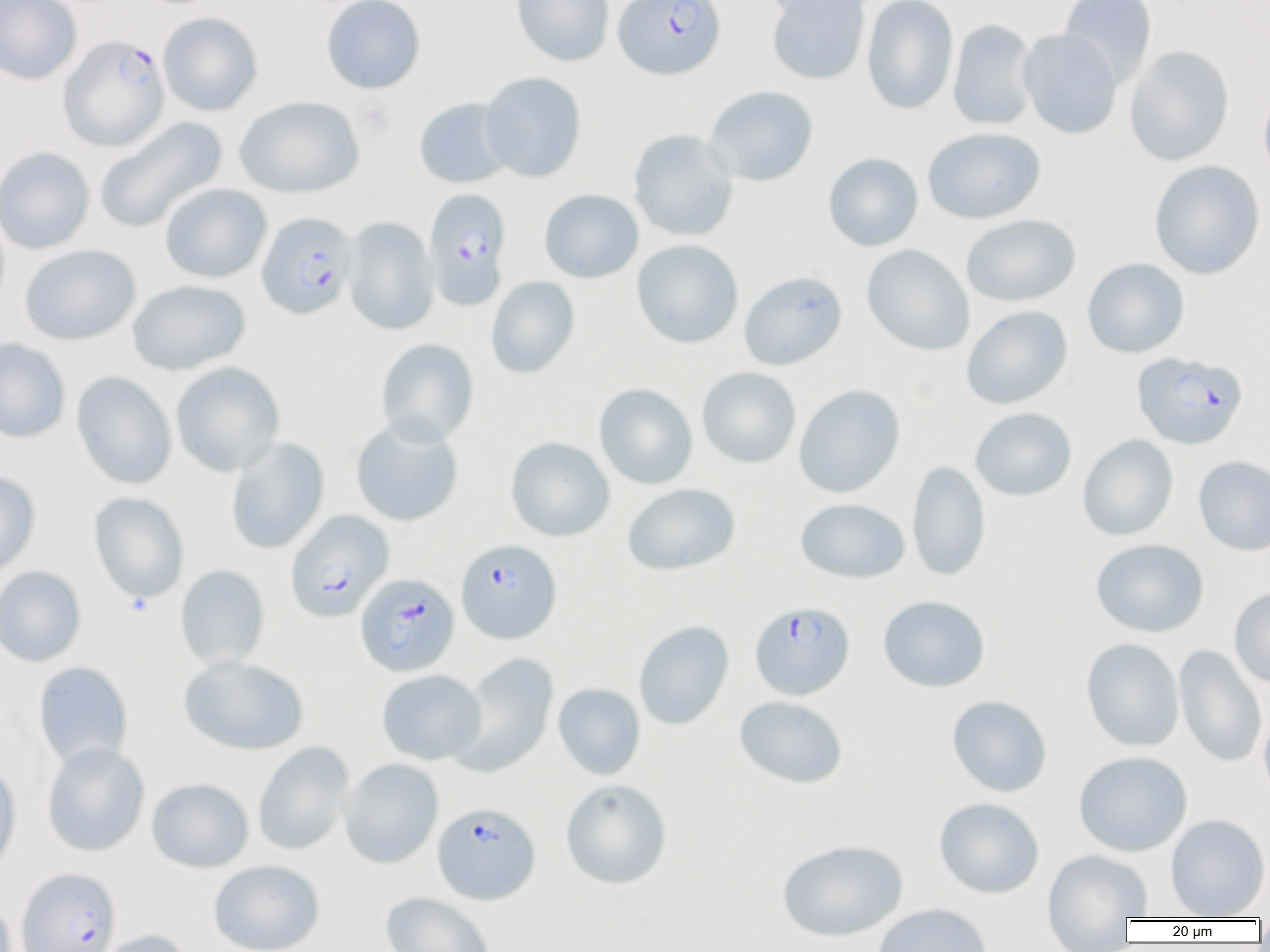 Approximate bounding boxes as (x1,y1)-(x2,y2) corner pairs in pixels. Plasmodium falciparum-infected red blood cell locations: (613,0)-(725,80), (58,34)-(169,151), (423,188)-(511,310), (256,212)-(358,319), (1132,351)-(1248,449), (285,509)-(393,623), (456,538)-(562,643), (355,573)-(459,677), (750,601)-(854,700), (432,802)-(541,904), (16,867)-(122,952). Platelet locations: (354,99)-(395,137). Uninfected red blood cell locations: (0,0)-(81,84), (321,0)-(425,93), (511,0)-(614,65), (766,0)-(871,85), (1059,0)-(1157,87), (862,1)-(959,114), (157,12)-(263,116), (947,19)-(1039,131), (1018,28)-(1122,138), (1124,45)-(1235,166), (479,72)-(586,182), (1258,82)-(1270,187), (704,85)-(818,187), (235,95)-(363,198), (414,98)-(513,188), (94,116)-(227,233), (922,127)-(1045,224), (628,128)-(739,242), (0,146)-(95,254), (823,152)-(923,251), (1150,160)-(1265,279), (160,183)-(272,283), (538,189)-(643,283), (961,214)-(1080,307), (343,216)-(440,335), (631,239)-(744,348), (19,244)-(141,345), (862,244)-(974,355), (1082,258)-(1189,358), (740,271)-(847,370), (486,275)-(580,379), (127,279)-(250,375), (961,305)-(1073,409), (0,338)-(71,443), (376,338)-(479,446), (170,362)-(285,476), (696,367)-(801,468), (71,371)-(176,489), (594,383)-(697,489), (794,384)-(905,497), (970,407)-(1077,501), (350,418)-(464,526), (1077,434)-(1178,540), (505,437)-(614,542), (225,438)-(329,554), (1194,455)-(1270,555), (906,460)-(991,581), (0,471)-(41,577), (622,482)-(740,575), (89,492)-(189,603), (795,498)-(910,583), (1090,538)-(1209,637), (0,565)-(87,667), (175,565)-(270,669), (1229,587)-(1270,688), (878,595)-(990,692), (634,620)-(734,730), (1082,638)-(1184,751), (1174,644)-(1267,767), (451,653)-(559,777), (178,655)-(309,755), (33,661)-(133,768), (376,669)-(486,765), (553,683)-(646,780), (734,695)-(848,789), (946,695)-(1052,797), (1258,709)-(1270,806), (42,741)-(150,856), (253,742)-(355,855), (1074,751)-(1193,857), (340,759)-(443,869), (0,760)-(22,877), (147,778)-(253,873), (560,778)-(672,889), (934,798)-(1044,898), (1165,814)-(1270,919), (777,838)-(908,941), (1042,848)-(1152,932), (208,859)-(325,952), (380,892)-(494,952), (872,903)-(993,952), (91,929)-(193,952). Slide-level diagnosis: Plasmodium falciparum. Thin blood smear. Optical microscopy. Image is 1270×952 pixels. Captured at 1000x magnification. Single field of view.